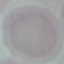
Summary:
  - Malaria status: uninfected
  - Image type: cell patch, automatically extracted from a larger field of view and resized to 64 × 64 pixels
  - Preparation: thin blood smear
  - Capture: smartphone camera at the microscope eyepiece
  - Stain: Giemsa